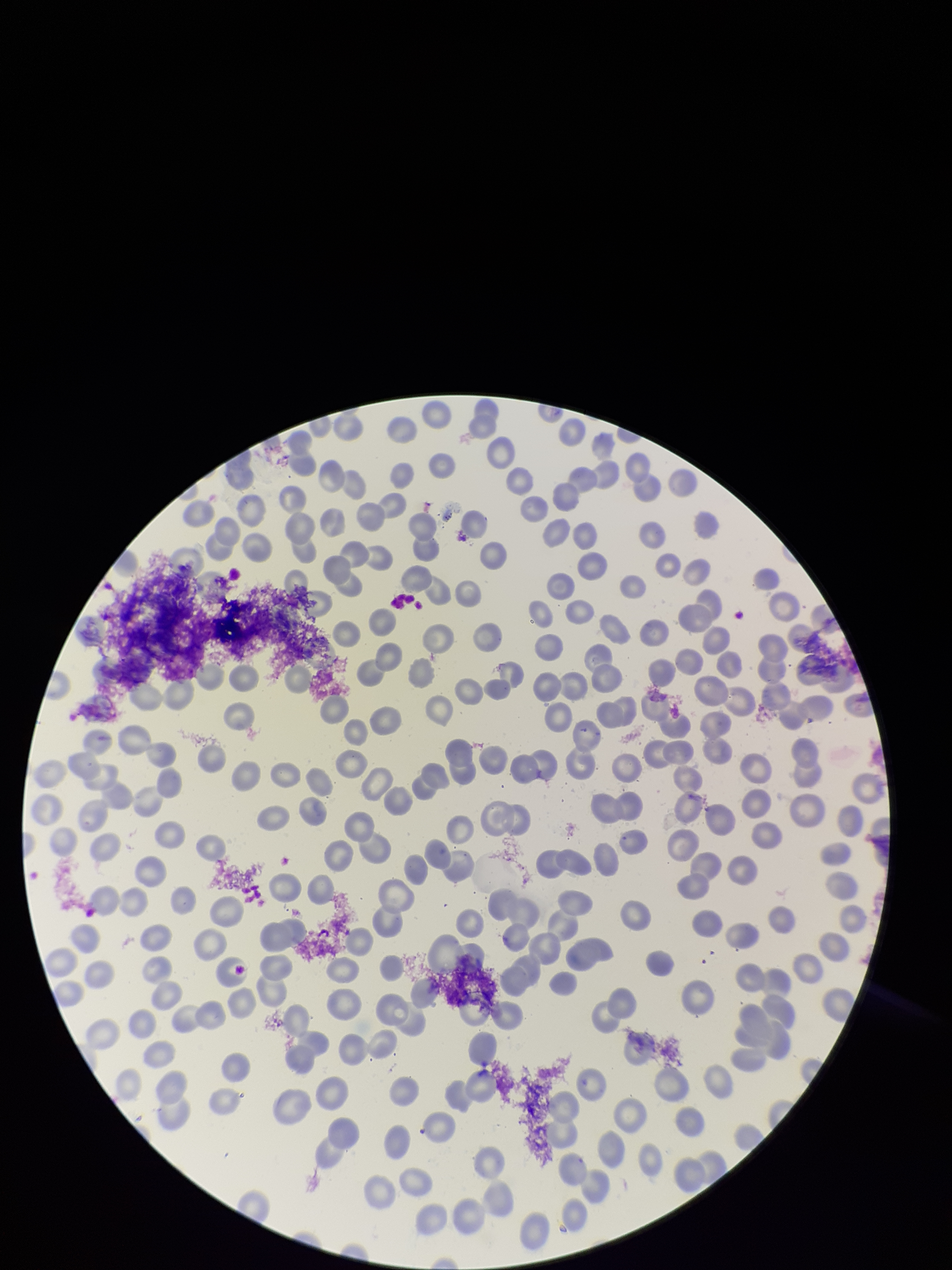
{
  "stain": "Giemsa",
  "preparation": "thin smear",
  "capture": "smartphone photograph through the microscope eyepiece",
  "field_of_view": "one from this slide",
  "parasitized_red_blood_cell_count": 0,
  "red_blood_cell_count": 229,
  "patient_malaria_status": "negative",
  "image_size": "952×1270 pixels",
  "parasitized_red_blood_cells": "none detected"
}